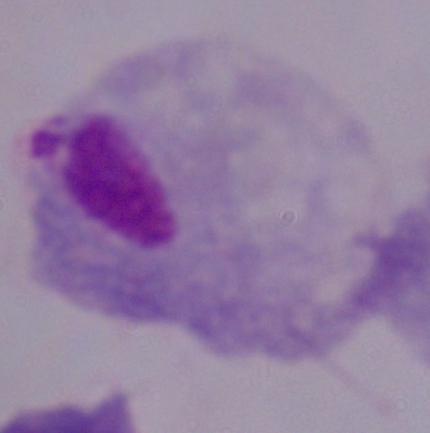
Summary:
  - Identification: trichomonad
  - Modality: micrograph
  - Magnification: 1000x